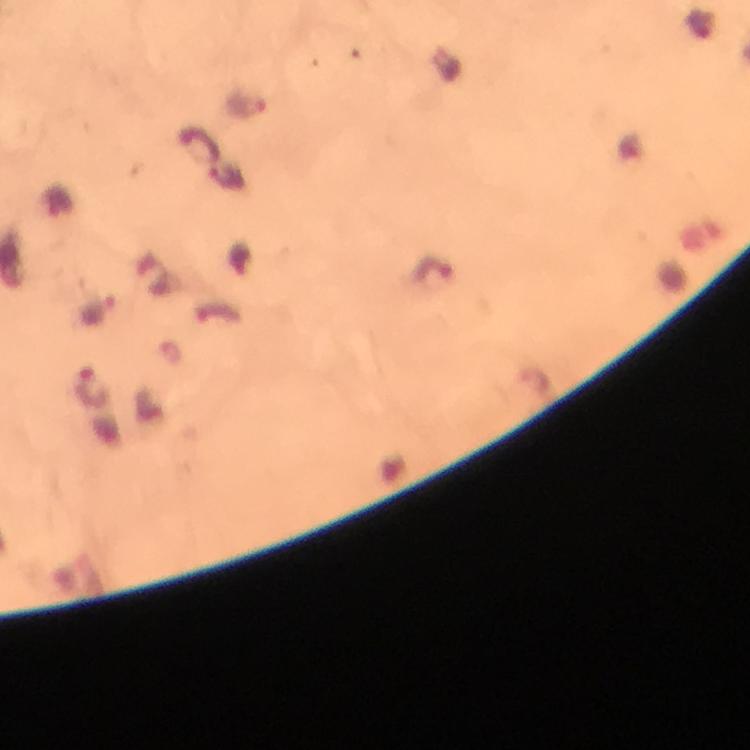
Approximate centers as (x, y) in pixels.
Summary:
  - Plasmodium parasite locations: (245, 103), (198, 144), (432, 270), (91, 389)
  - Capture: smartphone photograph through a microscope
  - Cropped from: a single field of view
  - Immersion oil: used
  - Magnification: 100x
  - Context: from a malaria diagnostic workup
  - Preparation: thick smear
  - Stain: Giemsa
  - Image size: 750×750 pixels